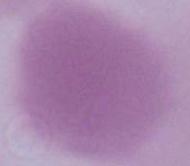

Summary:
  - Magnification: 1000x
  - Identification: red blood cell
  - Modality: photomicrograph